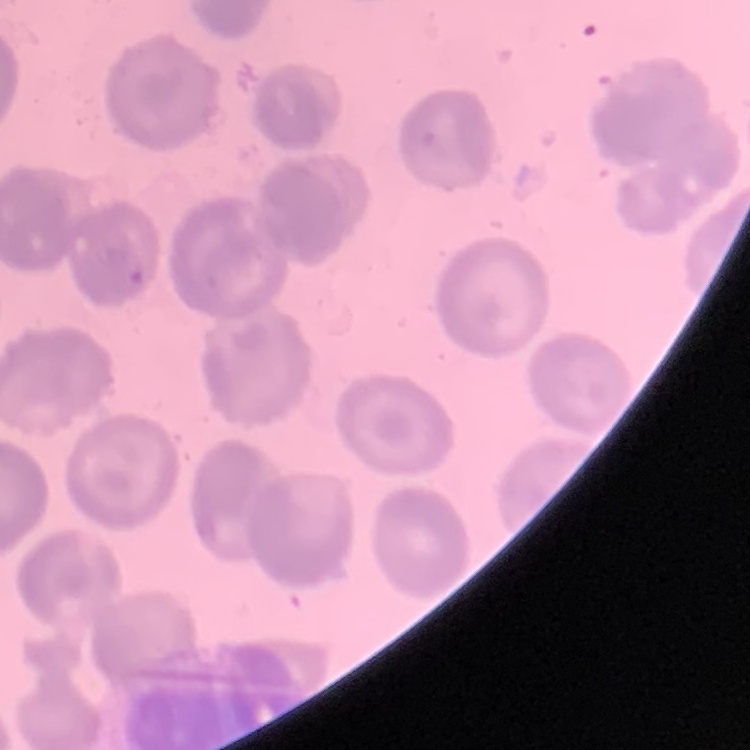

Summary:
  - Erythrocyte morphology: no rouleaux formation
  - Image type: one tile cut from a larger photomicrograph
  - Preparation: thin blood smear
  - Stain: Field's or Giemsa